Classify this cell by malaria status.
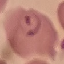

It is parasitized.

Summary:
  - Preparation: thin blood smear
  - Capture: smartphone camera at the microscope eyepiece
  - Image type: automatically extracted cell patch, resized to 64 × 64 pixels
  - Stain: Giemsa